Assess this cell for malaria.
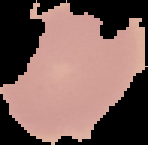
It is uninfected.

Image is 148×145 pixels. From a thin blood film. Cell region segmented out of the field of view; the surrounding area is masked to black.